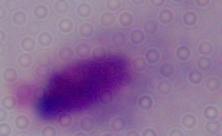

Summary:
  - Magnification: 1000x
  - Identification: trichomonad
  - Modality: photomicrograph